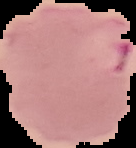 From a thin blood smear. Image is 136×148 pixels. The area outside the segmented cell region is set to black. Malaria status: parasitized.